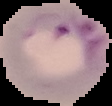
image type = segmented cell region on a black background
image size = 112×106 pixels
malaria status = parasitized
preparation = thin blood smear